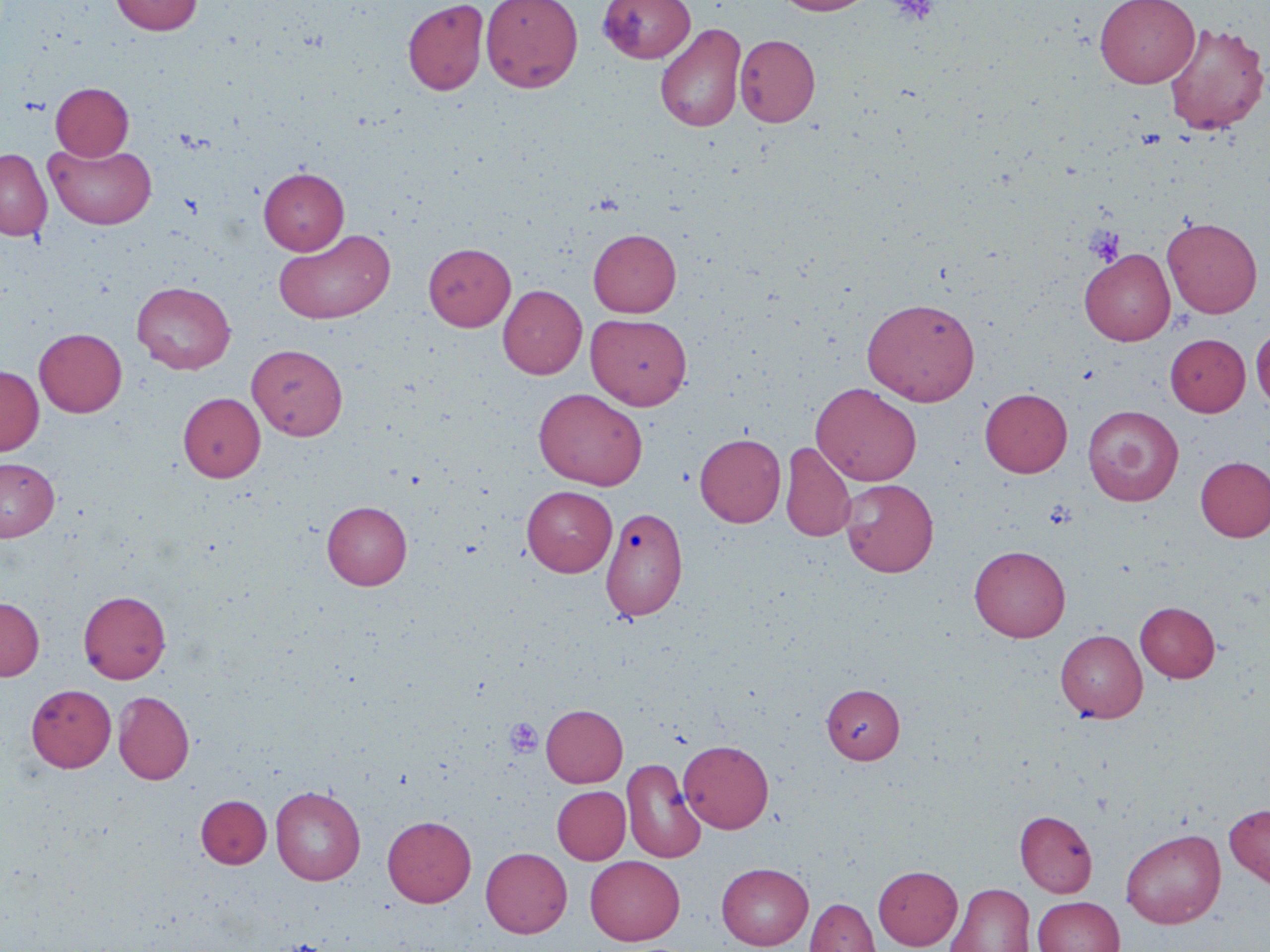

Approximate bounding boxes as (x1, y1, x2, y2) in pixels. Uninfected red blood cell locations: (110, 0, 202, 35), (402, 0, 489, 96), (481, 0, 583, 92), (598, 0, 696, 63), (775, 0, 877, 16), (1094, 0, 1200, 88), (1163, 21, 1269, 135), (655, 23, 746, 132), (735, 35, 820, 126), (51, 82, 133, 160), (44, 142, 157, 229), (0, 149, 52, 241), (258, 167, 349, 254), (1162, 217, 1263, 318), (274, 228, 395, 324), (588, 229, 681, 317), (424, 243, 516, 331), (1079, 248, 1175, 345), (132, 281, 236, 373), (498, 285, 586, 379), (862, 297, 980, 405), (586, 313, 692, 409), (1251, 326, 1270, 413), (34, 328, 127, 417), (1165, 333, 1250, 416), (246, 344, 348, 440), (0, 365, 44, 455), (811, 382, 922, 485), (533, 388, 647, 490), (979, 388, 1072, 477), (178, 392, 265, 482), (1082, 405, 1184, 506), (694, 433, 786, 527), (780, 441, 856, 543), (1196, 456, 1270, 542), (0, 457, 59, 541), (839, 479, 938, 577), (522, 486, 617, 576), (322, 501, 412, 590), (600, 507, 687, 622), (969, 545, 1070, 641), (78, 590, 170, 684), (0, 597, 44, 680), (1136, 602, 1220, 682), (1055, 629, 1147, 722), (26, 684, 116, 772), (821, 684, 904, 763), (113, 691, 194, 785), (541, 704, 628, 787), (679, 740, 774, 833), (622, 758, 706, 863), (271, 785, 366, 885), (552, 785, 630, 864), (196, 795, 271, 868), (1224, 803, 1270, 889), (1015, 810, 1097, 897), (382, 815, 476, 907), (1121, 828, 1225, 928), (481, 847, 572, 938), (585, 855, 685, 945), (716, 862, 814, 950), (873, 865, 962, 950), (945, 883, 1034, 952), (1033, 896, 1124, 952), (805, 899, 879, 952). Platelet locations: (886, 0, 940, 25), (1085, 227, 1124, 266), (504, 719, 543, 757). Slide-level diagnosis: negative for blood parasites. Captured at 1000x magnification. May-Grünwald-Giemsa-stained preparation. Image is 1270×952 pixels. Single field of view. Optical microscopy. Thin blood film.